State which cell type is depicted.
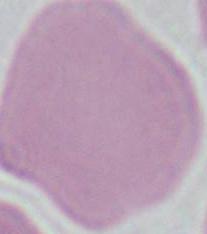

This is an erythrocyte.

{
  "modality": "photomicrograph",
  "magnification": "1000x"
}